Assess this cell for malaria.
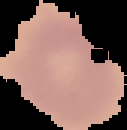
It is uninfected.

image size = 127×130 pixels
preparation = thin blood smear
image type = segmented cell region with the area outside set to black